Assess the morphology of the erythrocytes.
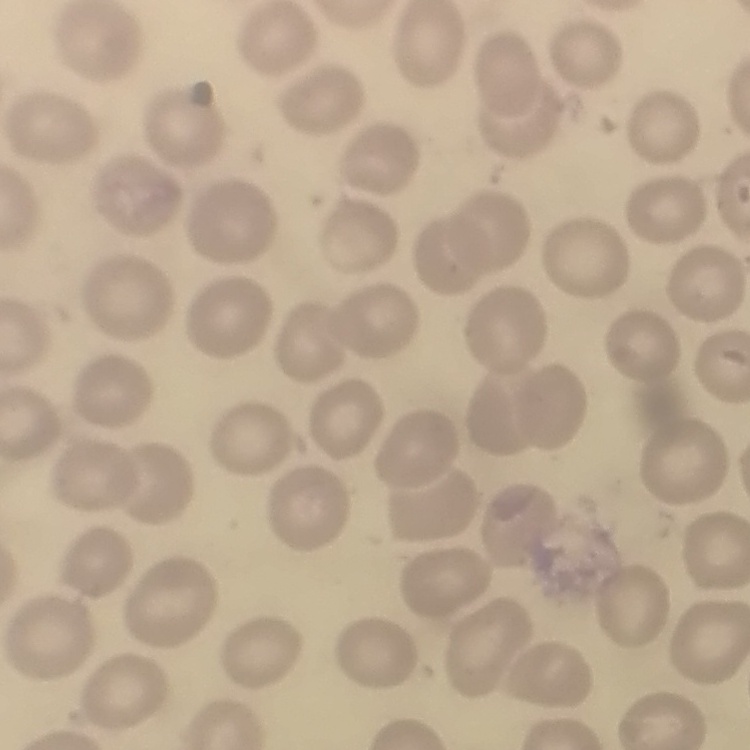

No rouleaux formation.

stain: Field's or Giemsa
image_type: one tile cut from a larger photomicrograph
preparation: thin peripheral smear